Point out each Plasmodium parasite and each leukocyte.
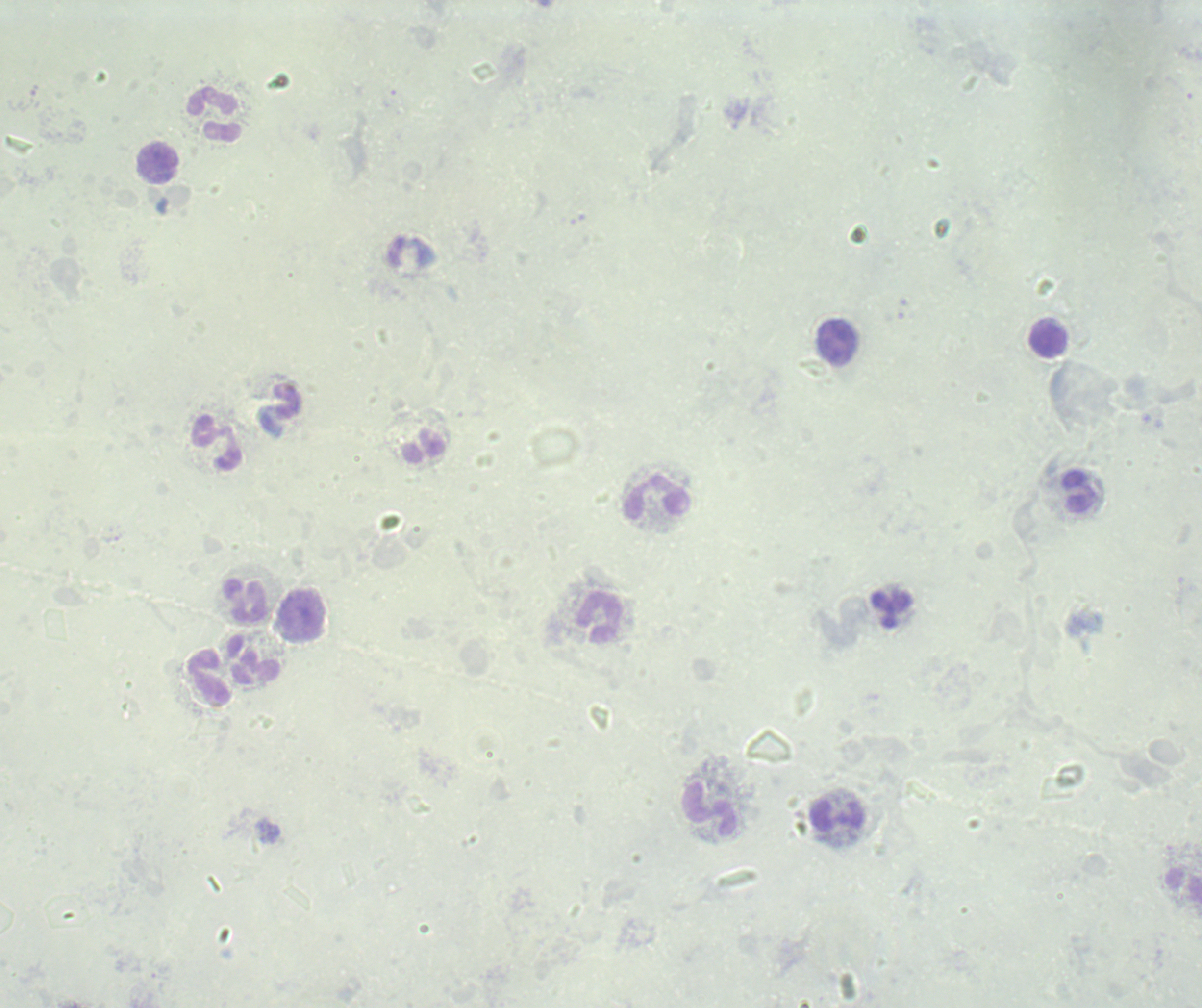
No Plasmodium parasites seen.
Approximate centers as [x, y] in pixels.
Leukocytes: [215, 114], [158, 162], [1048, 340], [216, 441], [1078, 492], [658, 497], [246, 601], [891, 609], [301, 614], [599, 615], [253, 660], [209, 678], [709, 809], [836, 816], [1183, 884].

Summary:
  - Image size: 1202×1008 pixels
  - Stain: Romanowsky
  - Context: previously used in a real diagnosis
  - Field of view: single
  - Preparation: thick smear of blood
  - Background quality: poor
  - Magnification: 100x